Comment on the morphology of the erythrocytes.
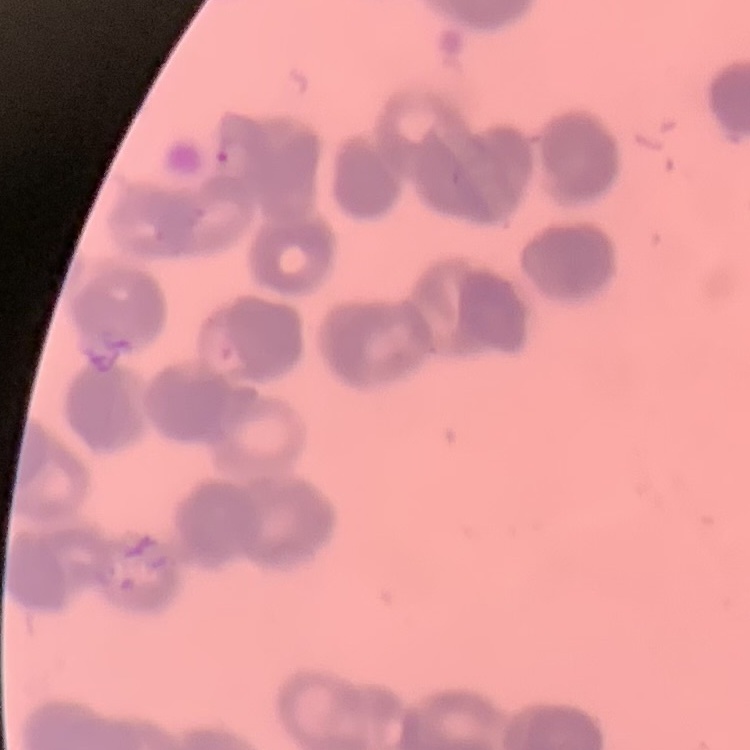
Rouleaux formation.

Summary:
  - Stain: Field's or Giemsa
  - Image type: one tile cut from a larger photomicrograph
  - Preparation: thin blood smear